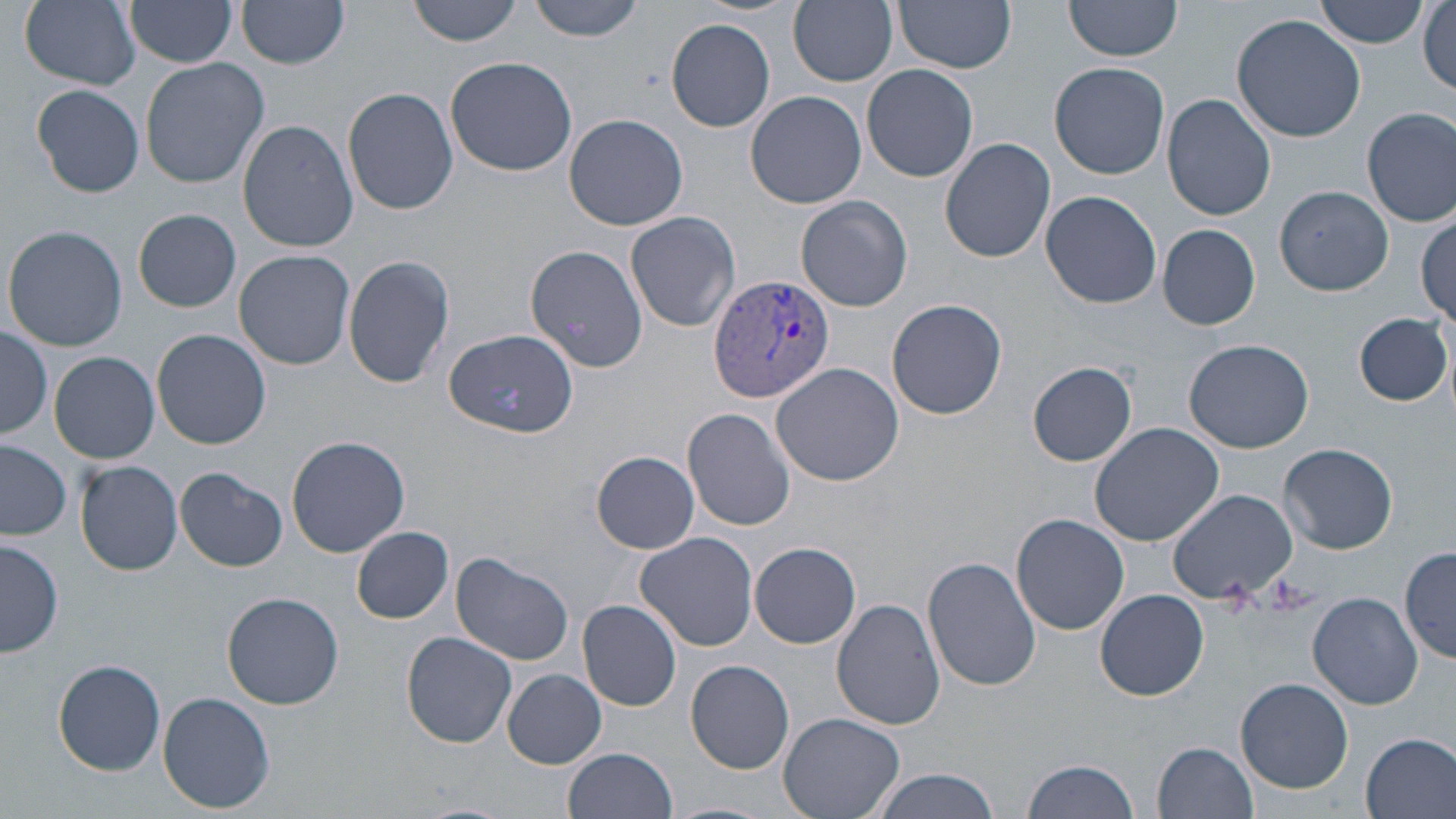 Approximate bounding boxes as named x1/y1/x2/y2 corners in pixels. Plasmodium vivax-infected red blood cell locations: (x1=709, y1=272, x2=836, y2=402). Uninfected red blood cell locations: (x1=18, y1=0, x2=141, y2=90), (x1=127, y1=0, x2=237, y2=69), (x1=409, y1=0, x2=523, y2=45), (x1=526, y1=0, x2=649, y2=41), (x1=788, y1=0, x2=898, y2=86), (x1=894, y1=0, x2=1018, y2=73), (x1=1064, y1=0, x2=1184, y2=61), (x1=1315, y1=0, x2=1428, y2=49), (x1=237, y1=2, x2=349, y2=70), (x1=1419, y1=2, x2=1455, y2=97), (x1=1231, y1=12, x2=1370, y2=142), (x1=666, y1=18, x2=776, y2=132), (x1=445, y1=57, x2=578, y2=176), (x1=141, y1=58, x2=270, y2=189), (x1=1050, y1=62, x2=1170, y2=178), (x1=861, y1=64, x2=979, y2=183), (x1=31, y1=83, x2=145, y2=198), (x1=342, y1=88, x2=458, y2=216), (x1=745, y1=91, x2=867, y2=209), (x1=1163, y1=94, x2=1276, y2=220), (x1=1362, y1=107, x2=1456, y2=227), (x1=564, y1=113, x2=690, y2=231), (x1=237, y1=119, x2=359, y2=252), (x1=939, y1=137, x2=1055, y2=263), (x1=1276, y1=185, x2=1393, y2=296), (x1=1041, y1=191, x2=1162, y2=310), (x1=795, y1=195, x2=913, y2=313), (x1=134, y1=208, x2=241, y2=312), (x1=626, y1=211, x2=740, y2=333), (x1=1416, y1=212, x2=1454, y2=325), (x1=1157, y1=223, x2=1261, y2=330), (x1=4, y1=225, x2=128, y2=353), (x1=526, y1=245, x2=649, y2=374), (x1=234, y1=250, x2=356, y2=370), (x1=345, y1=253, x2=456, y2=390), (x1=887, y1=298, x2=1008, y2=421), (x1=1355, y1=314, x2=1451, y2=406), (x1=0, y1=325, x2=52, y2=439), (x1=152, y1=329, x2=271, y2=449), (x1=445, y1=329, x2=578, y2=436), (x1=1183, y1=339, x2=1316, y2=453), (x1=47, y1=351, x2=159, y2=464), (x1=771, y1=361, x2=904, y2=485), (x1=1028, y1=361, x2=1138, y2=466), (x1=684, y1=408, x2=798, y2=531), (x1=1088, y1=422, x2=1224, y2=546), (x1=288, y1=435, x2=410, y2=557), (x1=0, y1=441, x2=72, y2=540), (x1=1279, y1=442, x2=1398, y2=554), (x1=592, y1=451, x2=698, y2=552), (x1=76, y1=461, x2=183, y2=576), (x1=173, y1=467, x2=288, y2=571), (x1=1168, y1=490, x2=1295, y2=604), (x1=1011, y1=514, x2=1130, y2=636), (x1=352, y1=526, x2=453, y2=623), (x1=635, y1=531, x2=760, y2=651), (x1=1, y1=537, x2=63, y2=659), (x1=750, y1=541, x2=861, y2=649), (x1=1401, y1=546, x2=1455, y2=665), (x1=451, y1=554, x2=573, y2=666), (x1=923, y1=556, x2=1042, y2=694), (x1=1096, y1=589, x2=1209, y2=701), (x1=223, y1=592, x2=343, y2=710), (x1=1307, y1=592, x2=1424, y2=710), (x1=578, y1=599, x2=681, y2=710), (x1=832, y1=599, x2=945, y2=730), (x1=402, y1=631, x2=517, y2=748), (x1=55, y1=658, x2=167, y2=775), (x1=685, y1=659, x2=794, y2=773), (x1=502, y1=670, x2=606, y2=768), (x1=1236, y1=678, x2=1354, y2=793), (x1=158, y1=690, x2=276, y2=813), (x1=779, y1=712, x2=905, y2=819), (x1=1360, y1=732, x2=1456, y2=819), (x1=1153, y1=741, x2=1260, y2=818), (x1=563, y1=748, x2=677, y2=819), (x1=1021, y1=757, x2=1139, y2=819), (x1=872, y1=771, x2=1004, y2=819), (x1=666, y1=801, x2=770, y2=819). Slide-level diagnosis: Plasmodium vivax. 1000x magnification. May-Grünwald-Giemsa stain. Image is 1456×819 pixels. Thin blood film. Light microscopy. Single field of view.